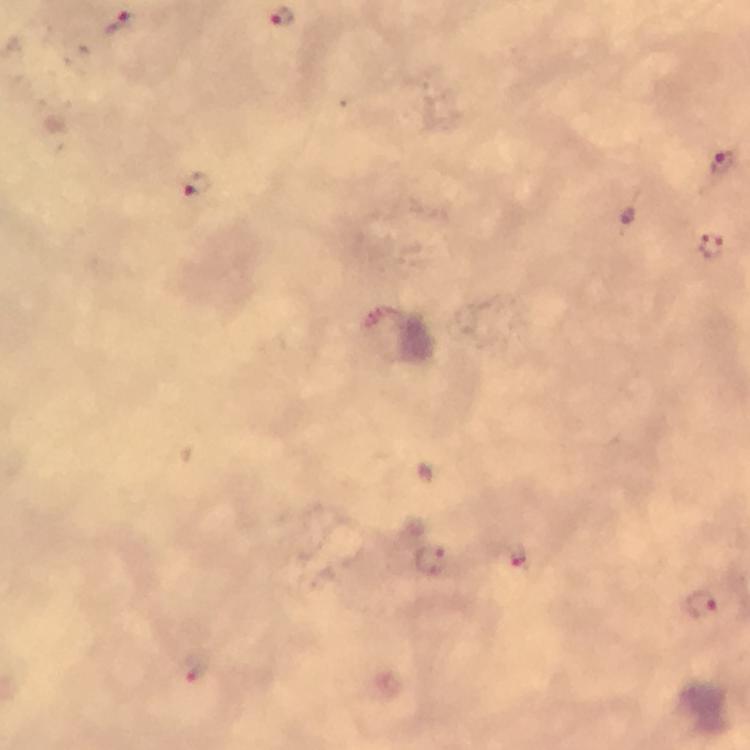

Approximate centers as [x, y] in pixels. Plasmodium parasite locations: [119, 22], [723, 162], [197, 185], [710, 247], [512, 556], [429, 563], [701, 604], [196, 669]. Giemsa-stained preparation. Immersion oil applied. Image is 750×750 pixels. Smartphone photograph taken through a microscope. 100x magnification. From a diagnostic examination for malaria. Cropped region of a single field of view. Thick blood film.